Identify the parasite.
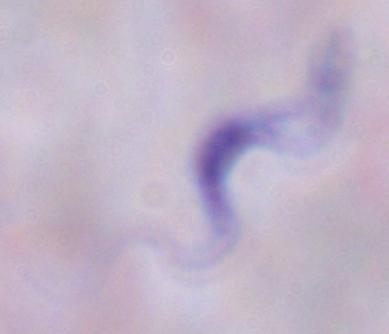

This is a trypanosome.

Summary:
  - Modality: photomicrograph
  - Magnification: 1000x